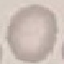
Summary:
  - Malaria status: uninfected
  - Stain: Giemsa
  - Preparation: thin blood smear
  - Image type: automatically extracted cell patch, resized to 64 × 64 pixels
  - Capture: smartphone camera at the microscope eyepiece